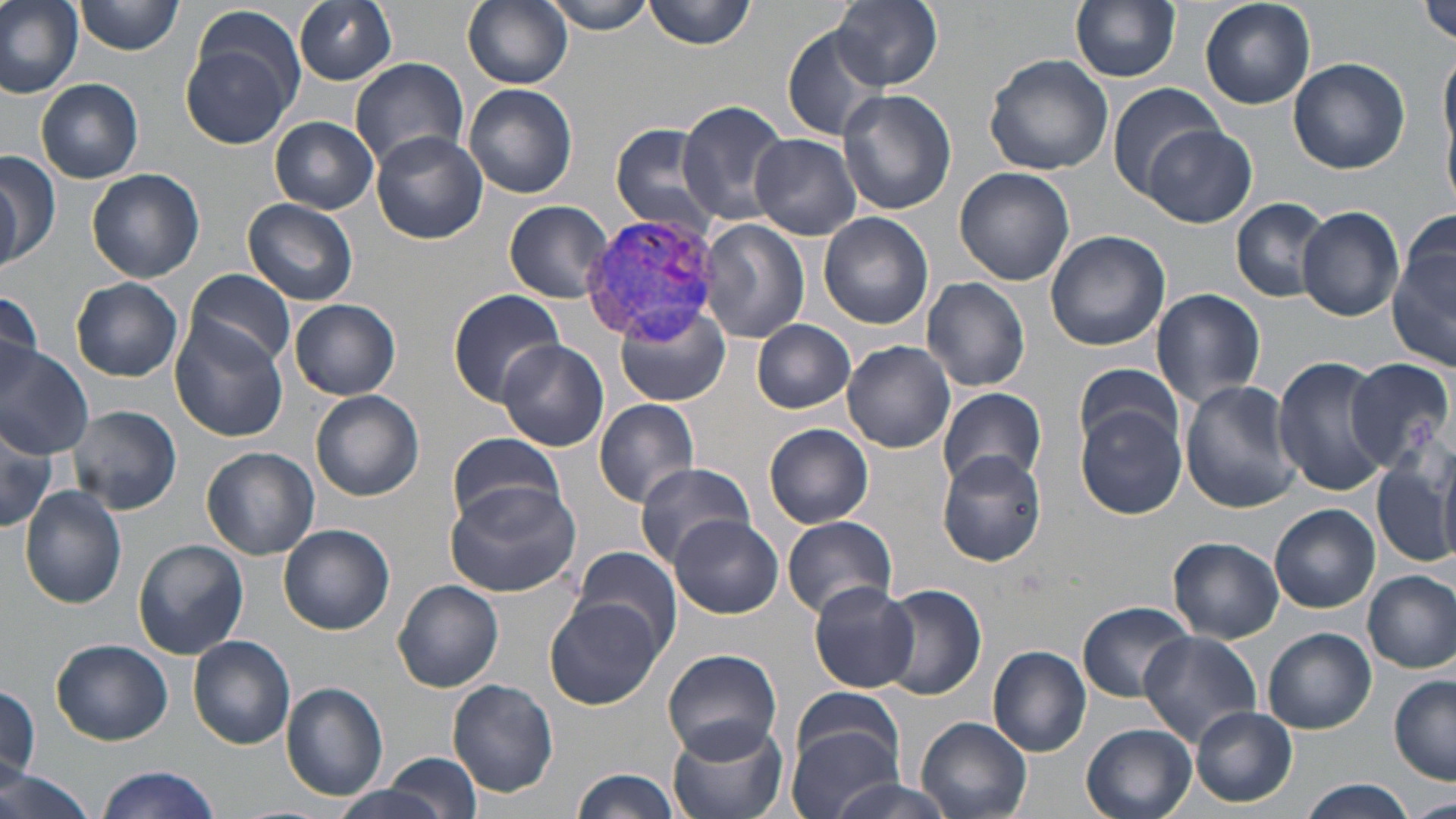
Summary:
  - Coordinate format: approximate bounding boxes as (x1,y1)-(x2,y2) corner pairs in pixels
  - Plasmodium vivax-infected red blood cell locations: (579,212)-(729,345)
  - Uninfected red blood cell locations: (0,0)-(83,98), (75,0)-(182,56), (295,0)-(397,85), (462,0)-(573,90), (544,0)-(654,34), (644,0)-(756,50), (833,0)-(943,90), (1071,0)-(1181,83), (1200,0)-(1315,110), (1420,1)-(1456,48), (783,26)-(889,143), (179,29)-(300,152), (1440,48)-(1455,161), (983,54)-(1114,177), (349,57)-(467,169), (1287,58)-(1411,175), (36,77)-(144,184), (1108,80)-(1228,194), (463,83)-(578,199), (838,90)-(958,216), (676,100)-(794,224), (271,116)-(379,213), (609,122)-(726,237), (1143,127)-(1256,229), (370,129)-(486,244), (750,133)-(861,241), (0,152)-(54,271), (953,167)-(1075,286), (86,168)-(205,281), (243,197)-(359,305), (1232,197)-(1333,302), (504,201)-(613,303), (1298,205)-(1405,322), (1400,208)-(1455,310), (818,212)-(934,329), (701,220)-(809,343), (1044,229)-(1169,352), (1387,250)-(1456,374), (186,268)-(296,370), (920,277)-(1030,392), (71,278)-(184,381), (0,287)-(41,385), (447,288)-(566,404), (1150,288)-(1267,409), (290,298)-(400,400), (617,307)-(732,406), (170,318)-(287,441), (752,319)-(857,413), (496,340)-(609,452), (843,340)-(953,454), (0,346)-(95,458), (1273,358)-(1393,496), (1344,359)-(1453,466), (1074,362)-(1184,451), (1180,381)-(1302,513), (936,386)-(1046,492), (309,390)-(425,502), (594,398)-(700,506), (69,406)-(183,513), (1075,406)-(1188,520), (0,413)-(57,538), (764,424)-(874,528), (446,432)-(564,526), (202,447)-(321,561), (1438,447)-(1456,561), (1372,449)-(1454,569), (937,451)-(1050,567), (633,461)-(753,566), (443,481)-(582,597), (20,486)-(127,608), (1269,503)-(1379,613), (669,514)-(783,618), (782,515)-(898,618), (1168,521)-(1380,631), (278,524)-(394,634), (1167,537)-(1285,643), (133,540)-(248,658), (568,548)-(687,656), (1363,570)-(1456,672), (392,580)-(503,691), (808,581)-(919,693), (875,583)-(987,701), (545,598)-(664,709), (1079,602)-(1195,702), (1263,628)-(1376,733), (1138,630)-(1262,748), (189,636)-(294,748), (51,640)-(172,746), (988,647)-(1092,756), (661,648)-(782,760), (1389,675)-(1455,784), (447,679)-(559,797), (1,682)-(41,782), (280,682)-(389,802), (793,687)-(902,776), (1189,706)-(1299,808), (916,716)-(1032,819), (668,720)-(789,819), (1079,723)-(1199,819), (788,724)-(901,818), (384,750)-(482,819), (0,765)-(94,819), (94,765)-(221,819), (572,767)-(681,819), (822,775)-(960,819), (1300,778)-(1415,819), (327,783)-(455,819), (1410,796)-(1456,819)
  - Platelet locations: (1403,415)-(1443,452)
  - Slide-level diagnosis: Plasmodium vivax
  - Magnification: 1000x
  - Field of view: one of a larger specimen
  - Preparation: thin blood smear
  - Stain: May-Grünwald-Giemsa
  - Modality: light microscopy
  - Image size: 1456×819 pixels